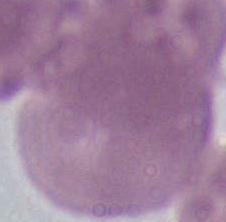
Photomicrograph. An erythrocyte is shown. Captured at 1000x magnification.